Name the parasite shown.
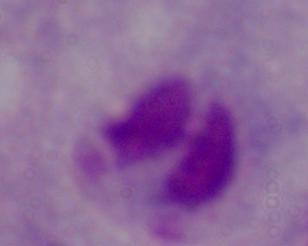

A trichomonad.

magnification = 1000x
modality = photomicrograph